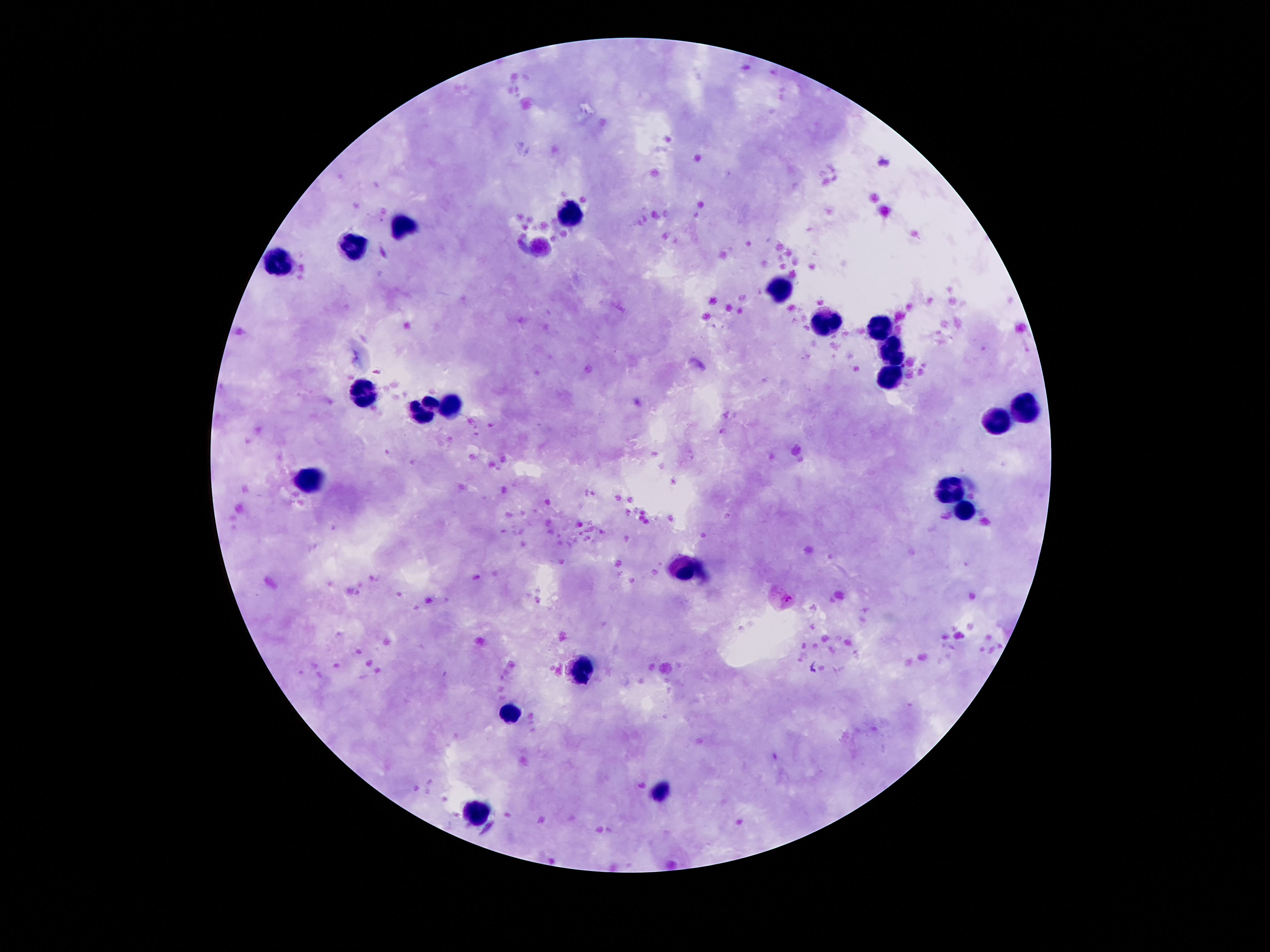
Approximate centers as [x, y] in pixels. Leukocyte locations: [573, 212], [403, 226], [353, 248], [279, 260], [779, 290], [828, 324], [880, 327], [892, 349], [892, 376], [361, 394], [450, 403], [1026, 406], [428, 408], [999, 422], [306, 479], [949, 490], [966, 511], [687, 571], [581, 670], [509, 711], [660, 791], [477, 814]. Photographed through the microscope eyepiece with a smartphone camera. Single field of view. Thick blood smear. 100x magnification. Patient malaria status: not infected. Image is 1270×952 pixels. Giemsa-stained preparation.